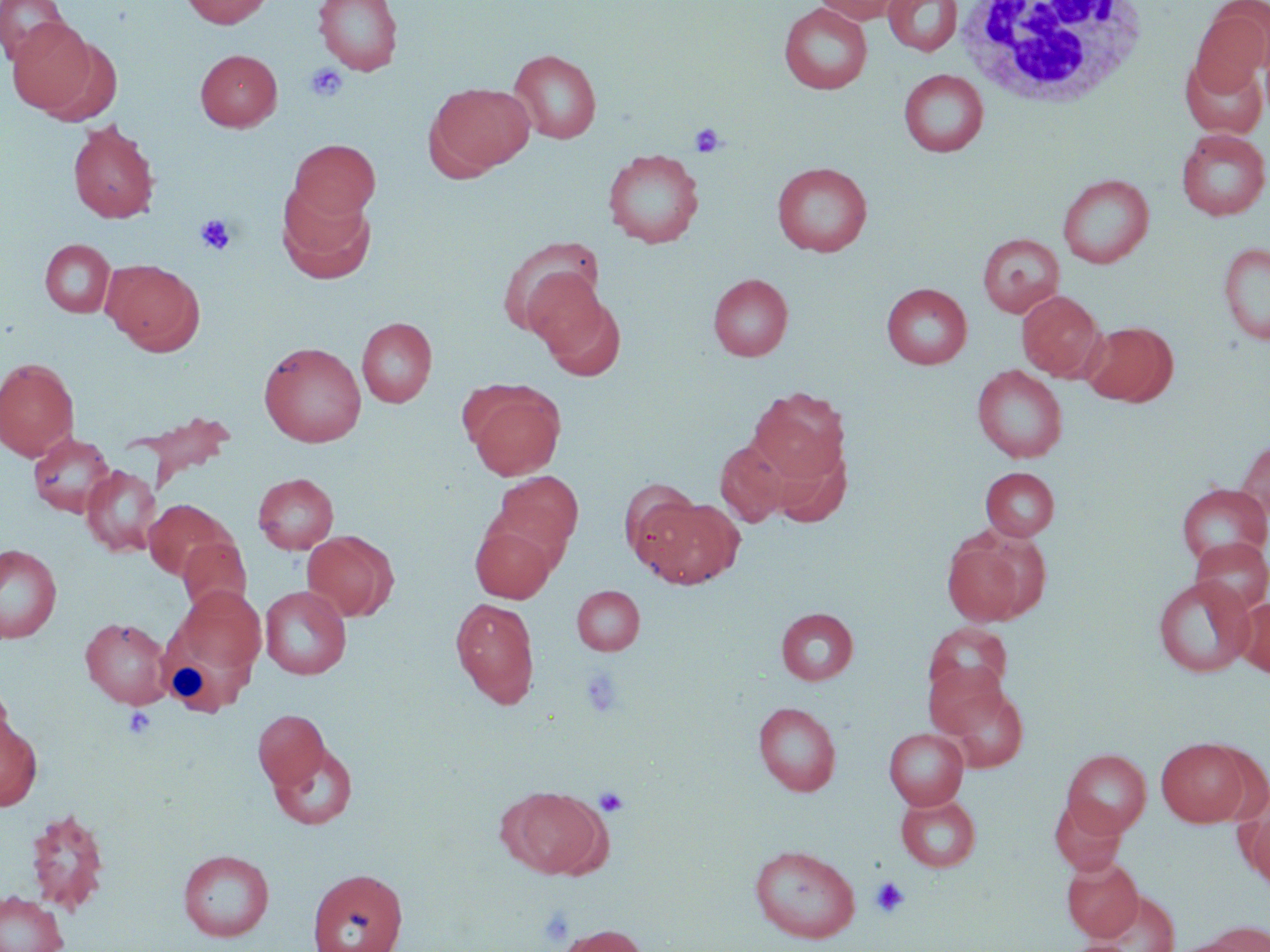
slide-level diagnosis = no evidence of blood parasites
stain = May-Grünwald-Giemsa
preparation = thin blood film
modality = optical microscopy
magnification = 1000x
uninfected red blood cell locations = approximate bounding boxes as (x1,y1)-(x2,y2) corner pairs in pixels: (0,0)-(69,66), (181,0)-(273,28), (313,0)-(403,75), (812,0)-(906,25), (883,0)-(963,56), (778,3)-(873,94), (1191,6)-(1270,96), (7,17)-(97,115), (37,36)-(123,127), (195,49)-(282,131), (509,49)-(602,143), (1181,55)-(1268,138), (899,69)-(988,157), (428,83)-(535,176), (67,121)-(159,223), (1176,128)-(1270,220), (289,140)-(380,222), (602,148)-(704,248), (772,162)-(872,257), (1057,173)-(1154,268), (278,185)-(376,283), (977,233)-(1065,317), (500,238)-(606,341), (40,239)-(115,318), (1218,243)-(1270,346), (102,258)-(204,354), (708,273)-(793,360), (881,283)-(972,369), (533,287)-(626,380), (1017,290)-(1106,381), (356,317)-(437,407), (1080,322)-(1178,407), (259,341)-(366,447), (0,358)-(79,460), (971,365)-(1068,463), (465,383)-(565,480), (747,386)-(849,485), (28,432)-(115,517), (715,439)-(789,527), (1235,441)-(1270,524), (81,465)-(161,556), (980,466)-(1059,540), (492,471)-(583,564), (253,473)-(338,554), (620,479)-(704,567), (1176,482)-(1270,568), (638,495)-(743,588), (144,499)-(234,581), (470,522)-(557,602), (301,530)-(397,622), (941,534)-(1036,627), (177,537)-(252,617), (1189,537)-(1269,615), (0,543)-(62,643), (1152,576)-(1254,677), (178,585)-(267,673), (260,585)-(352,679), (572,585)-(645,655), (450,597)-(539,707), (1234,598)-(1270,678), (776,607)-(858,684), (80,617)-(172,708), (156,623)-(265,716), (924,623)-(1013,702), (921,661)-(1014,744), (0,677)-(15,765), (936,680)-(1029,773), (752,702)-(841,796), (253,709)-(330,790), (0,714)-(43,812), (883,728)-(969,809), (1156,737)-(1253,827), (270,742)-(358,830), (1061,748)-(1151,837), (502,785)-(612,878), (896,794)-(982,872), (1049,797)-(1126,875), (1241,800)-(1270,891), (26,807)-(111,915), (749,844)-(860,942), (178,849)-(274,941), (1061,856)-(1144,941), (307,868)-(408,952), (1087,890)-(1181,952), (0,891)-(68,952), (1204,921)-(1270,952), (556,924)-(648,952), (1162,935)-(1257,952), (1063,940)-(1134,952)
white blood cell locations = approximate bounding boxes as (x1,y1)-(x2,y2) corner pairs in pixels: (953,1)-(1153,108)
field of view = single
platelet locations = approximate bounding boxes as (x1,y1)-(x2,y2) corner pairs in pixels: (305,62)-(349,102), (689,122)-(726,157), (195,214)-(237,255), (581,669)-(625,718), (124,706)-(156,739), (594,786)-(629,817), (870,876)-(910,918), (539,907)-(575,946)
image size = 1270×952 pixels